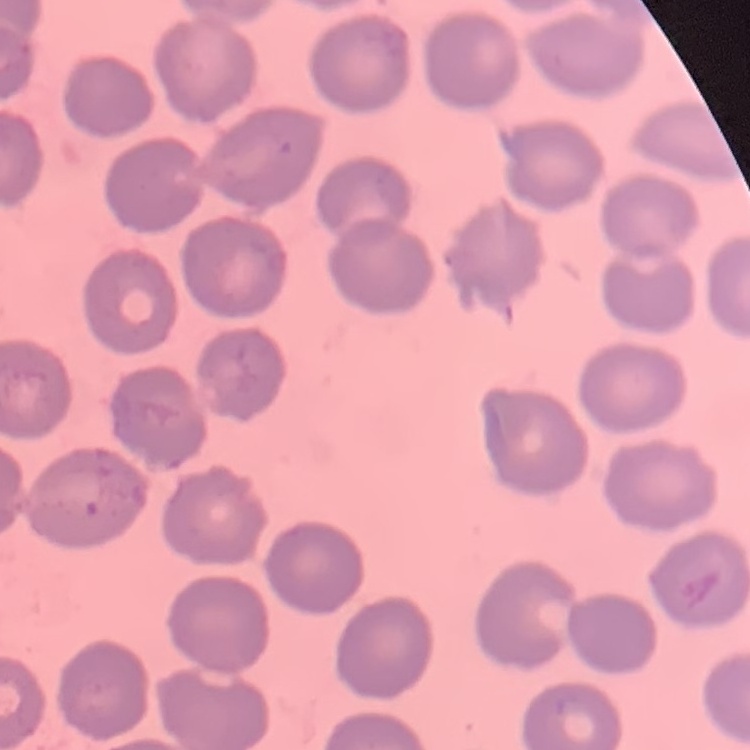
The erythrocytes exhibit no rouleaux formation. Thin blood film. Square crop of a larger photomicrograph. Stained with either Field's or Giemsa.